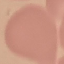
Summary:
  - Result: no malaria parasites seen
  - Image type: cell patch, automatically extracted from a larger field of view and resized to 64 × 64 pixels
  - Preparation: thin blood smear
  - Stain: Giemsa
  - Capture: smartphone camera at the microscope eyepiece